Report the malaria status of this cell.
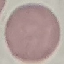

It is uninfected.

capture = smartphone camera at the microscope eyepiece
preparation = thin blood film
stain = Giemsa
image type = cell patch, automatically extracted from a larger field of view and resized to 64 × 64 pixels